Give the preparation type.
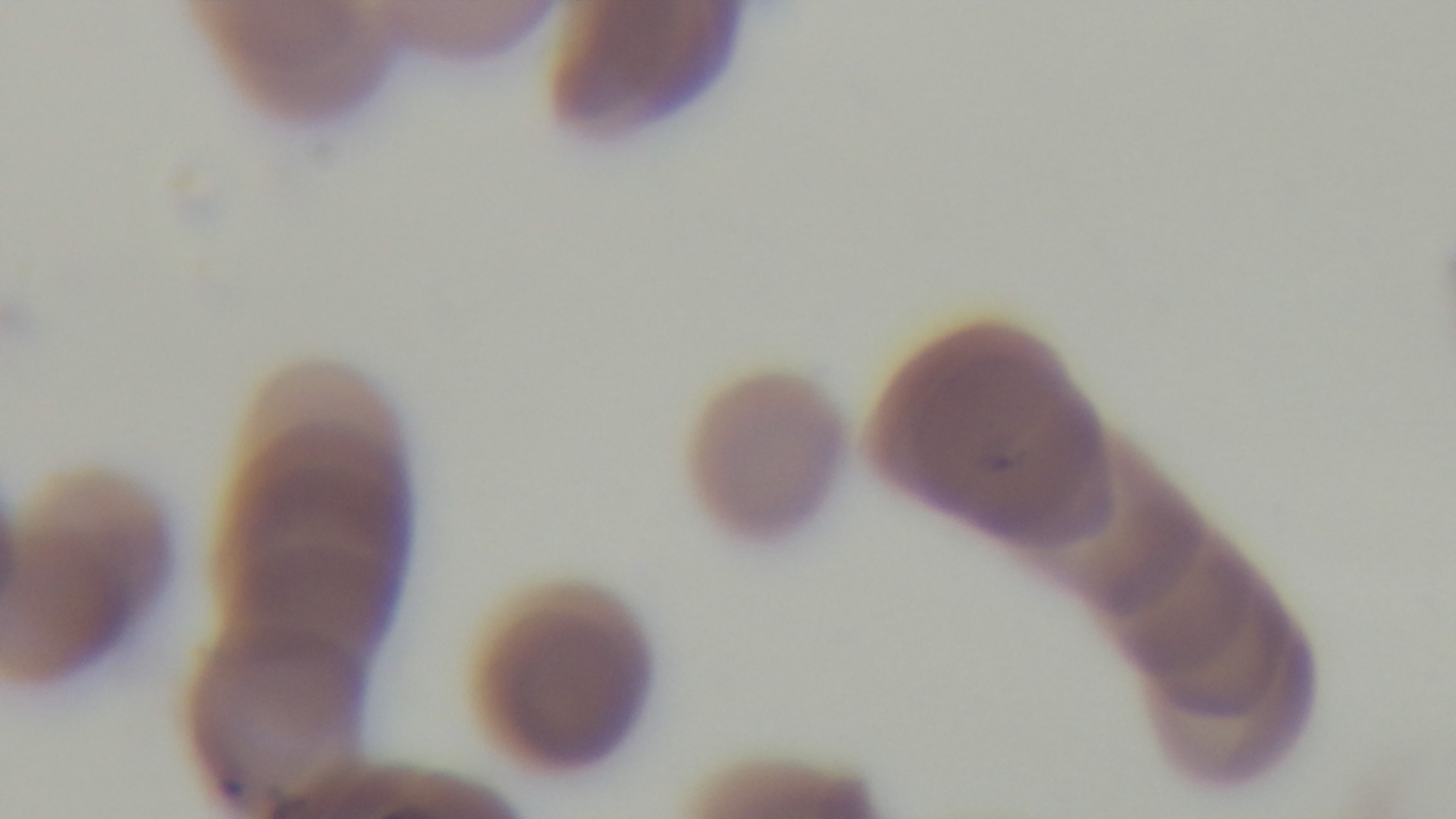

A thin smear.

Summary:
  - Malaria status: infected
  - Objective: 100x oil immersion
  - Stain: Giemsa
  - Capture: mounted 4K digital camera
  - Field of view: one from the slide
  - Modality: light microscopy